Identify the preparation type.
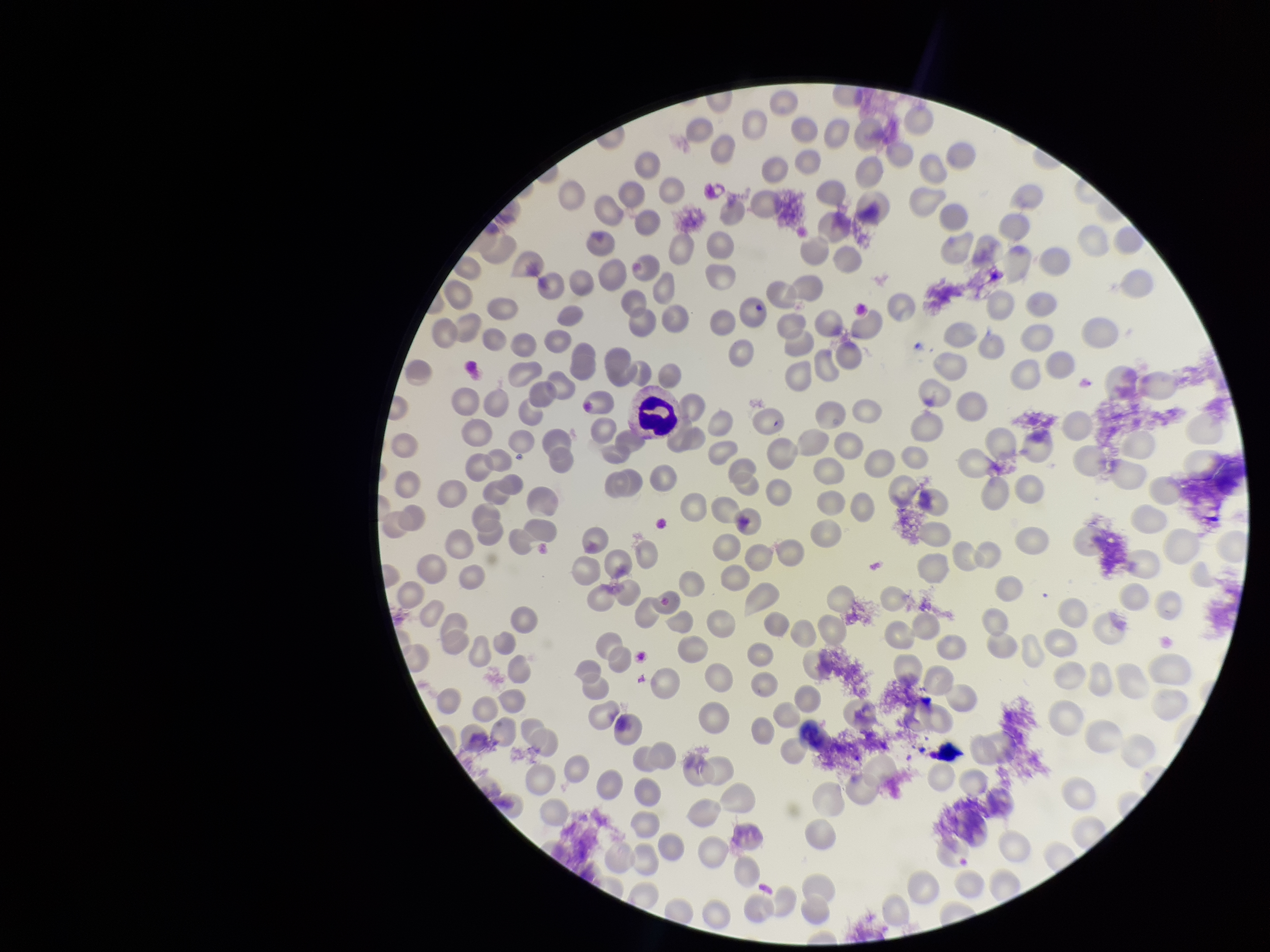
It is a thin blood smear.

Summary:
  - Capture: smartphone photograph through the microscope eyepiece
  - Patient malaria status: negative
  - Parasitized red blood cell count: 0
  - Parasitized red blood cells: none seen
  - Field of view: single
  - Stain: Giemsa
  - Image size: 1270×952 pixels
  - Red blood cell count: 224